State the preparation type.
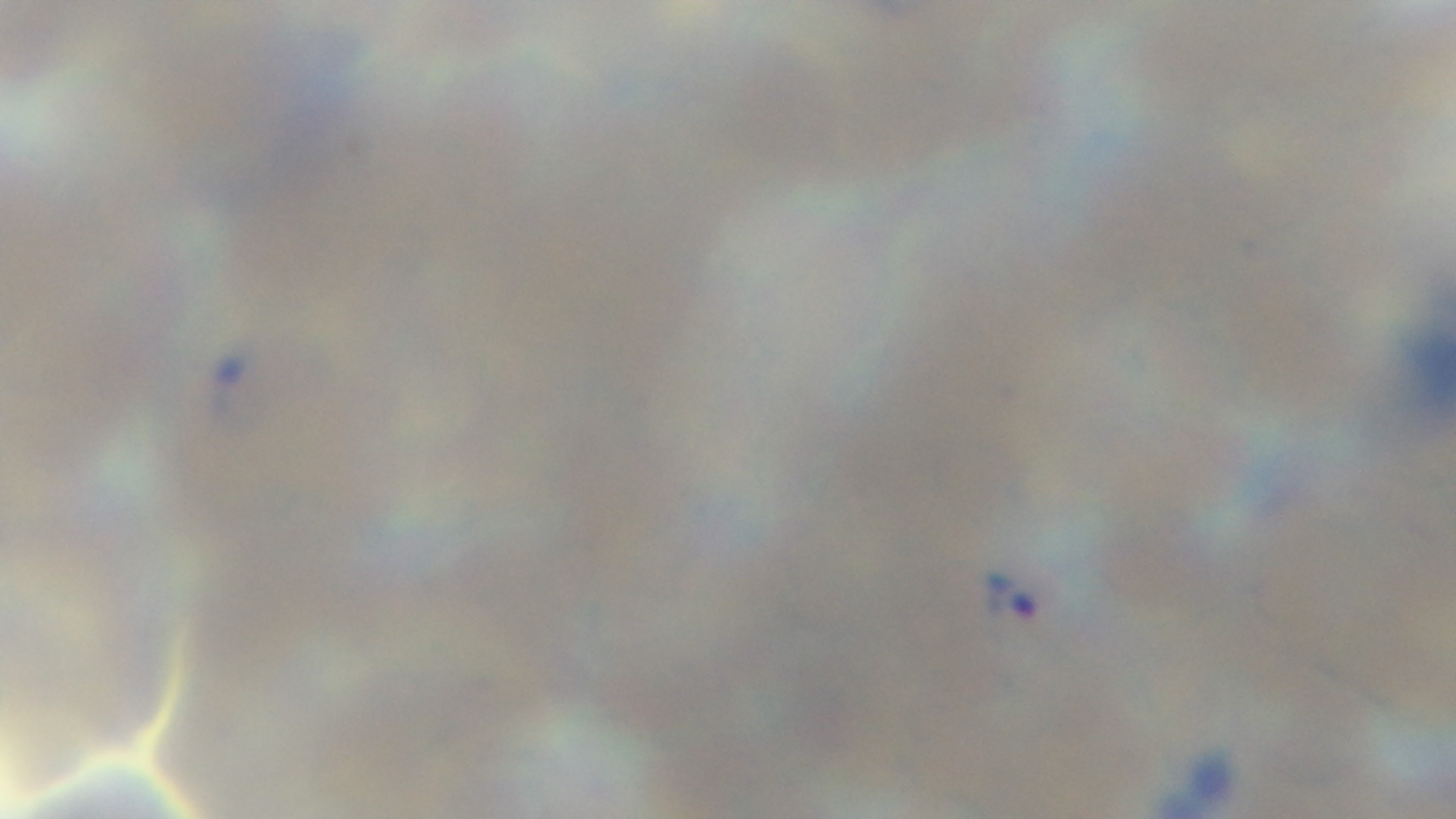
It is a thin blood film.

Summary:
  - Objective: 100x oil immersion
  - Capture: mounted 4K digital camera
  - Field of view: one from the slide
  - Malaria status: positive
  - Stain: Giemsa
  - Modality: light microscopy